Outline each Plasmodium parasite.
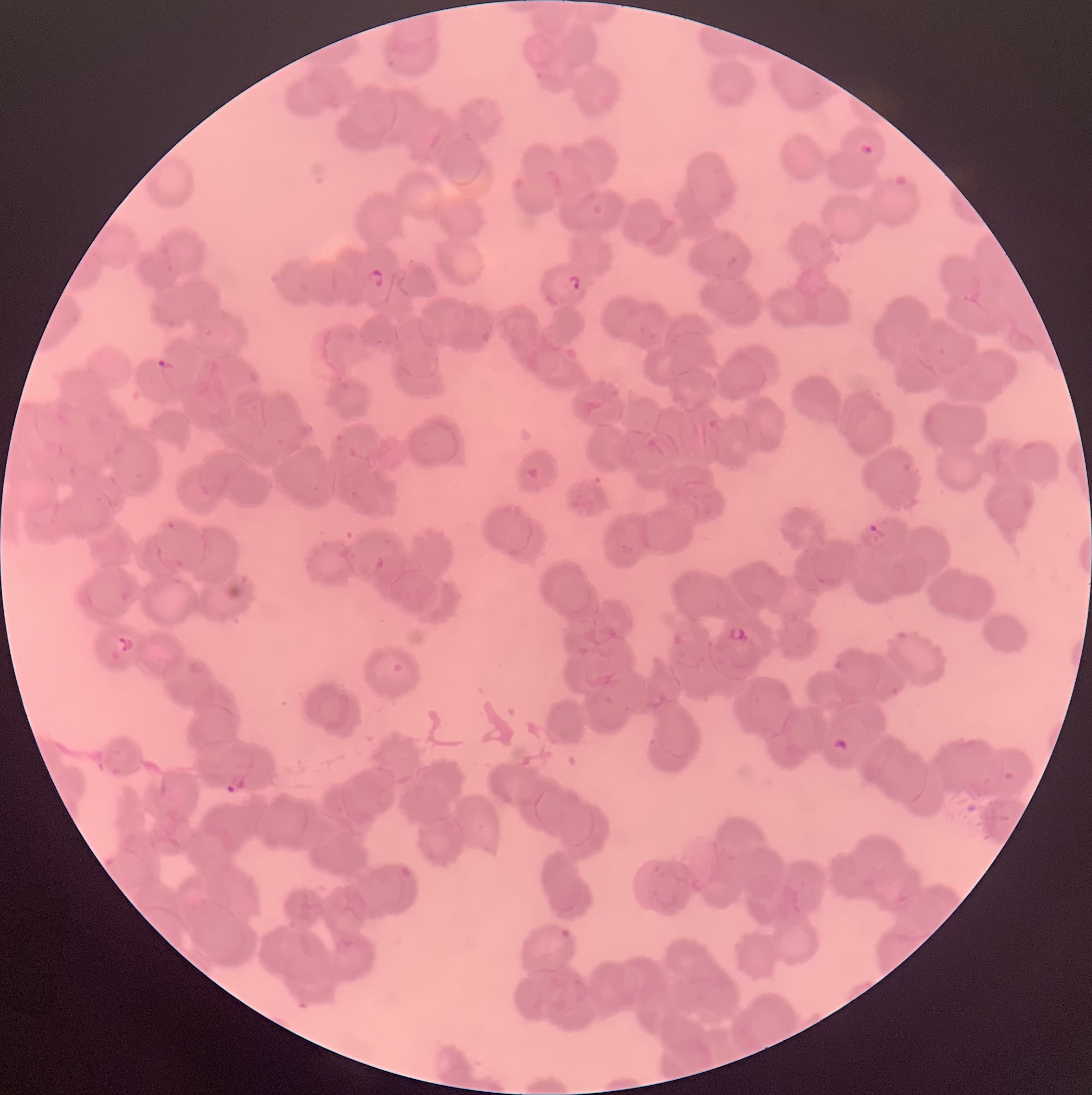
Approximate bounding boxes as (x1,y1)-(x2,y2) corner pairs in pixels.
Plasmodium parasites: (859,144)-(873,156), (366,269)-(383,288), (566,275)-(583,293), (156,359)-(175,374), (867,525)-(885,539), (375,556)-(384,568), (728,628)-(745,641), (116,636)-(133,652), (833,738)-(848,751), (225,775)-(245,793), (561,930)-(573,956), (572,980)-(588,1004).

Thin blood smear. Image is 1092×1095 pixels. Light microscopy. The red blood cells show rouleaux formation.